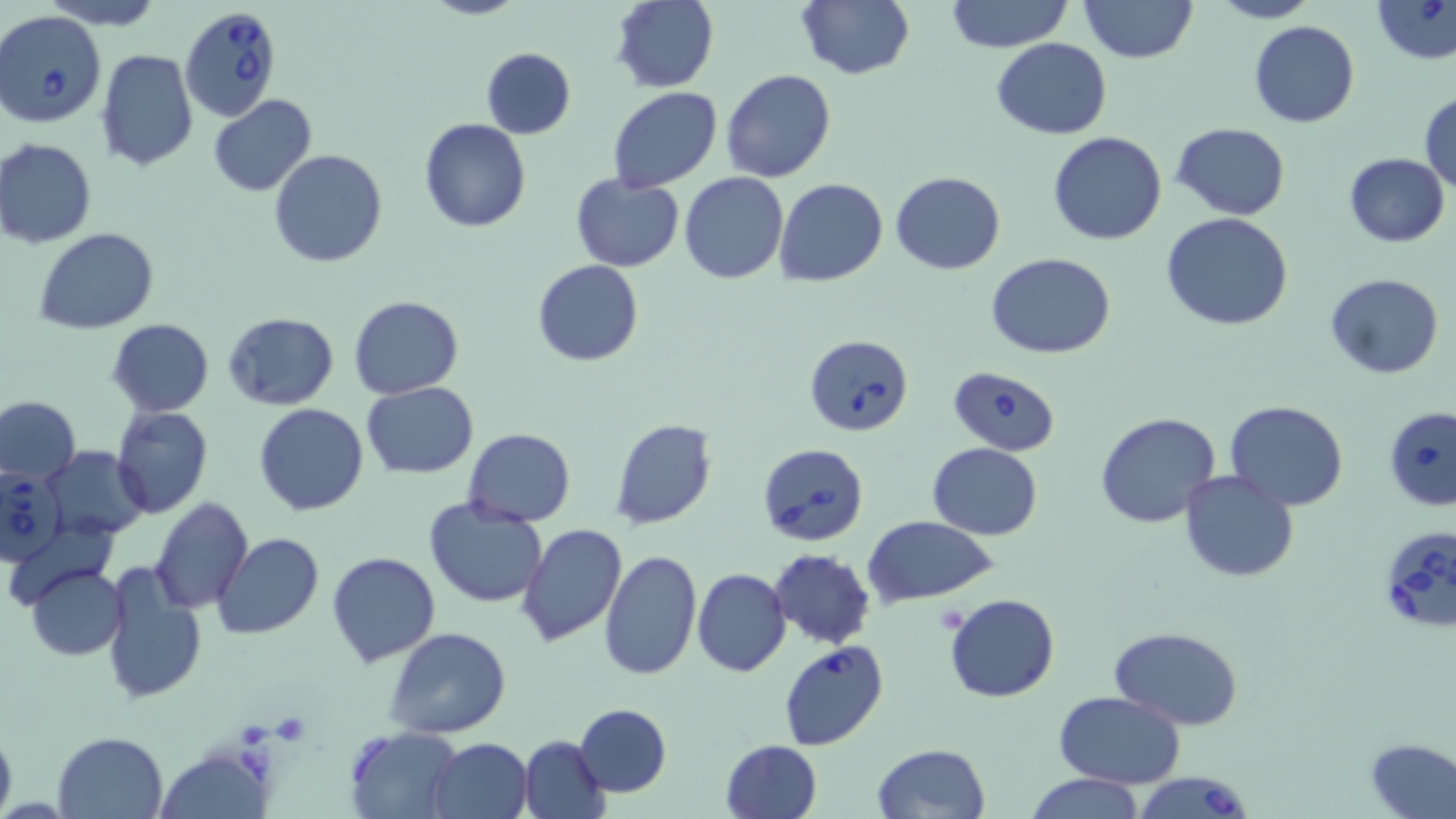
slide-level diagnosis = Babesia divergens
uninfected red blood cell locations = approximate bounding boxes as (x1,y1)-(x2,y2) corner pairs in pixels: (43,0)-(166,29), (610,0)-(719,93), (944,0)-(1073,52), (1079,0)-(1198,65), (1207,0)-(1322,24), (1372,0)-(1456,66), (794,1)-(916,81), (1248,19)-(1359,128), (991,37)-(1111,139), (479,47)-(575,139), (97,48)-(199,172), (721,69)-(836,182), (608,88)-(722,191), (1419,90)-(1456,193), (208,95)-(317,195), (420,119)-(531,234), (1172,122)-(1290,219), (1047,132)-(1167,245), (0,138)-(97,248), (267,149)-(388,268), (1343,152)-(1450,247), (890,171)-(1006,274), (680,173)-(788,285), (569,174)-(685,271), (775,179)-(888,287), (1161,212)-(1295,331), (35,229)-(159,334), (987,253)-(1116,359), (532,259)-(644,367), (1325,273)-(1443,379), (348,295)-(464,400), (222,311)-(339,411), (107,319)-(214,415), (360,382)-(478,479), (0,397)-(80,484), (1225,399)-(1348,511), (253,403)-(371,517), (111,406)-(214,520), (1095,411)-(1223,530), (608,417)-(718,530), (462,428)-(577,526), (926,443)-(1043,539), (44,446)-(148,541), (1179,470)-(1299,582), (423,496)-(548,607), (150,497)-(253,613), (864,516)-(1000,607), (516,523)-(627,648), (210,534)-(325,639), (597,548)-(702,683), (768,549)-(876,648), (326,551)-(441,669), (98,561)-(207,704), (25,564)-(127,661), (693,567)-(791,677), (945,593)-(1059,703), (386,627)-(512,739), (1111,627)-(1244,728), (1054,692)-(1186,788), (574,703)-(671,797), (0,721)-(17,819), (343,725)-(464,818), (53,731)-(168,818), (518,735)-(610,818), (428,737)-(534,819), (1366,737)-(1456,818), (719,739)-(823,819), (871,743)-(991,819), (157,749)-(267,819), (1026,773)-(1144,818)
field of view = one of a larger specimen
platelet locations = approximate bounding boxes as (x1,y1)-(x2,y2) corner pairs in pixels: (931,604)-(972,636), (271,713)-(313,744)
magnification = 1000x
preparation = thin blood smear
image size = 1456×819 pixels
Babesia divergens-infected red blood cell locations = approximate bounding boxes as (x1,y1)-(x2,y2) corner pairs in pixels: (180,3)-(281,122), (0,10)-(107,128), (802,334)-(913,437), (949,365)-(1059,456), (1382,406)-(1456,510), (755,443)-(870,548), (0,465)-(66,563), (1375,524)-(1456,637), (778,641)-(889,751), (1130,772)-(1255,819)
stain = May-Grünwald-Giemsa
modality = light microscopy